Give the position of every Plasmodium parasite and every leukocyte.
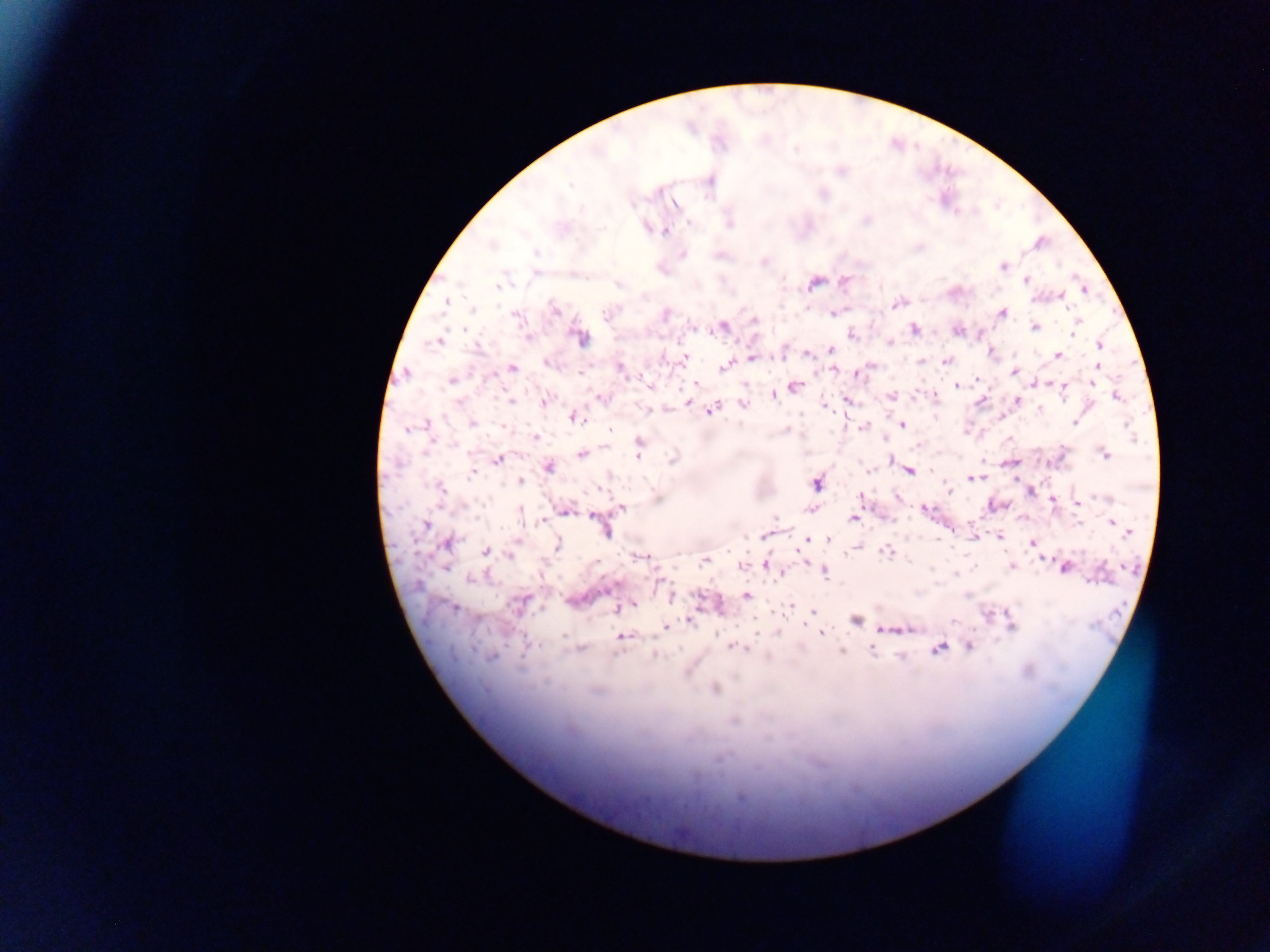

Approximate centers as x y in pixels.
Plasmodium parasites: 570 184; 632 205; 690 223; 729 223; 646 227; 665 231; 1040 243; 491 244; 536 253; 682 255; 720 255; 764 261; 1003 267; 1026 280; 815 283; 618 285; 498 286; 880 287; 1083 290; 1061 296; 446 302; 898 304; 473 310; 554 310; 1002 313; 607 314; 665 315; 833 315; 517 317; 754 320; 1075 325; 723 327; 1034 327; 915 330; 957 332; 1074 332; 852 334; 528 338; 579 339; 438 341; 889 343; 1099 345; 831 350; 991 352; 807 355; 1058 355; 751 357; 684 358; 946 361; 921 362; 547 363; 1098 366; 512 367; 723 367; 868 367; 621 369; 835 370; 1013 371; 857 375; 977 379; 452 381; 1039 382; 1092 383; 956 385; 1055 385; 650 386; 793 388; 1064 388; 774 395; 891 396; 915 396; 934 396; 1116 396; 600 398; 846 400; 511 401; 544 401; 982 401; 1018 401; 688 402; 743 404; 825 407; 714 409; 1039 409; 648 410; 574 417; 1002 417; 1074 422; 426 423; 473 423; 1126 424; 902 425; 863 427; 407 428; 610 430; 536 437; 640 445; 582 453; 638 453; 1105 454; 672 459; 498 460; 892 461; 1008 462; 548 467; 476 469; 909 471; 931 471; 472 474; 972 477; 520 481; 816 483; 439 488; 948 489; 861 495; 1106 498; 1052 500; 1077 502; 621 508; 810 509; 925 509; 565 511; 594 517; 852 519; 424 524; 1114 524; 1120 529; 604 530; 1128 532; 765 536; 999 537; 806 540; 828 540; 1032 543; 449 544; 557 545; 856 548; 486 551; 887 551; 510 555; 642 557; 705 560; 765 564; 742 565; 1011 566; 1065 568; 931 569; 824 571; 1103 573; 956 574; 780 575; 470 579; 670 595; 747 596; 519 604; 633 605; 790 606; 453 609; 617 609; 812 611; 987 614; 856 620; 689 621; 1012 626; 666 628; 905 628; 886 629; 821 632; 563 635; 622 637; 528 644; 970 647; 737 648; 938 648; 580 649; 871 650; 655 655; 901 656; 491 657; 1028 671; 715 688; 733 721; 741 797.
No leukocytes observed.

Image is 1270×952 pixels. Thick blood smear. Mobile-phone photograph taken through the microscope. One field of view. Collected in Ghana.